Report the malaria status of this cell.
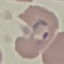
It is parasitized.

Summary:
  - Preparation: thin blood smear
  - Image type: automatically extracted cell patch, resized to 64 × 64 pixels
  - Capture: smartphone camera at the microscope eyepiece
  - Stain: Giemsa